Report the malaria status of this cell.
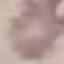

It is uninfected.

Summary:
  - Preparation: thin blood film
  - Capture: smartphone camera at the microscope eyepiece
  - Stain: Giemsa
  - Image type: automatically extracted cell patch, resized to 64 × 64 pixels